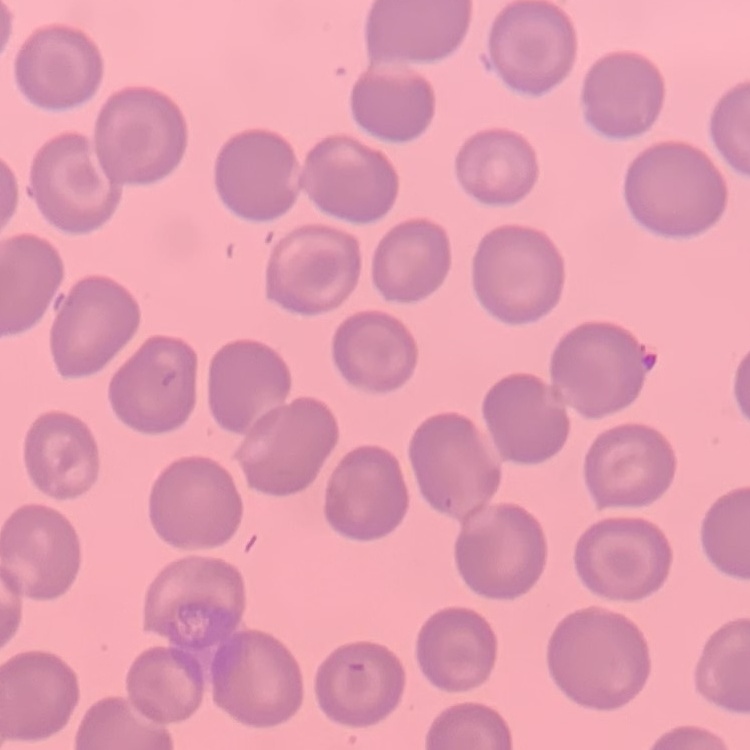
red blood cell morphology = no rouleaux formation
stain = Field's or Giemsa
image type = square crop of a larger photomicrograph
preparation = thin blood film